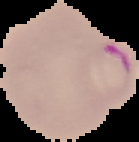

Result: malaria parasites identified. From a thin blood film. Cell region segmented out of the field of view; the surrounding area is masked to black. Image is 139×142 pixels.